Classify this cell by malaria status.
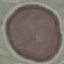
Uninfected.

Summary:
  - Stain: Giemsa
  - Preparation: thin blood smear
  - Capture: smartphone through the microscope eyepiece
  - Image type: cell patch, automatically extracted from a larger field of view and resized to 64 × 64 pixels